Outline each Plasmodium ovale-infected red blood cell.
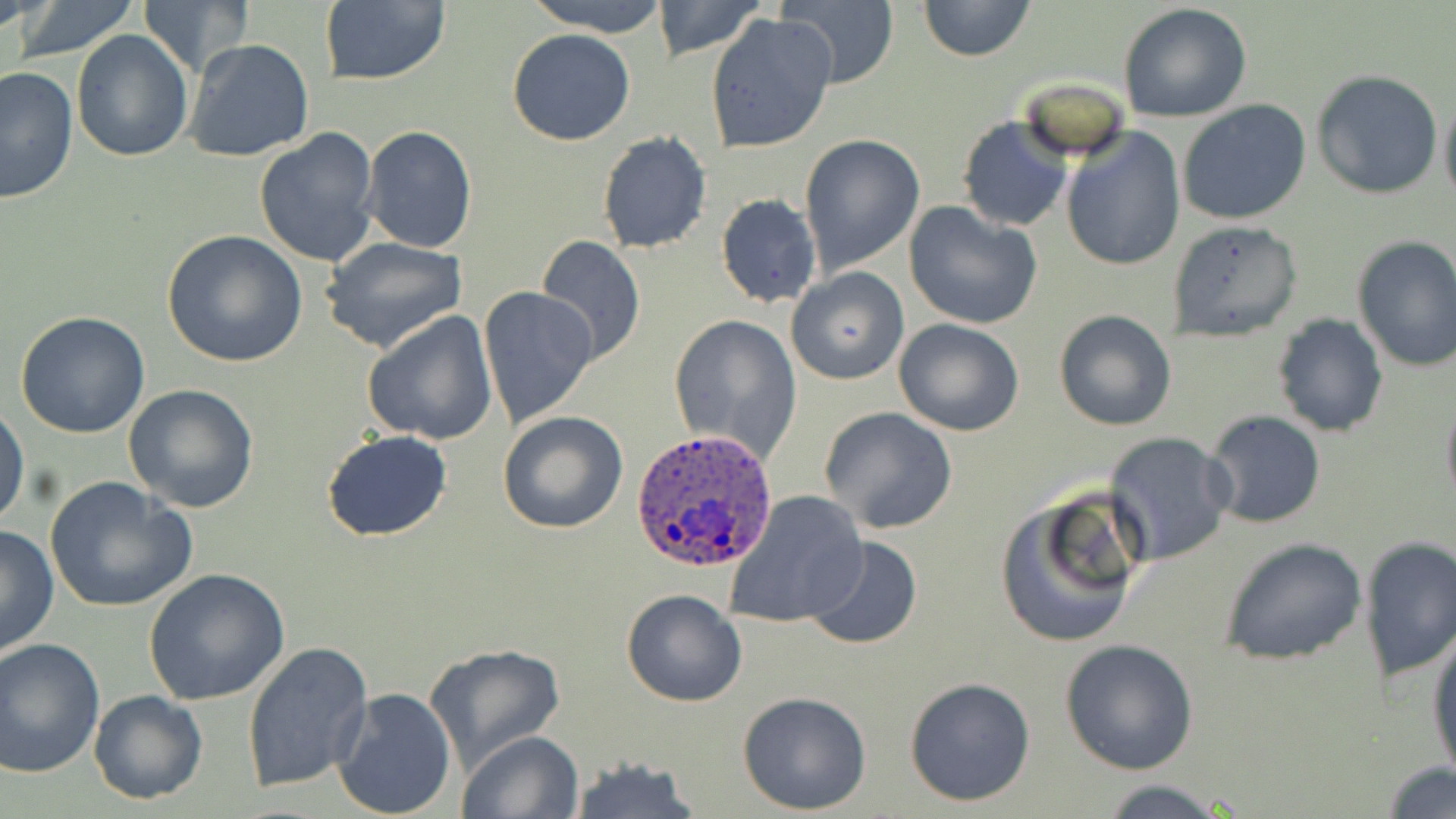

Approximate bounding boxes as (x1,y1)-(x2,y2) corner pairs in pixels.
Plasmodium ovale-infected red blood cells: (629,430)-(778,572).

Summary:
  - Uninfected red blood cell locations: (11,0)-(144,61), (524,0)-(676,36), (650,0)-(767,60), (918,0)-(1036,63), (139,1)-(251,73), (317,1)-(452,87), (777,1)-(897,86), (1118,2)-(1254,124), (704,12)-(837,154), (507,29)-(636,146), (70,30)-(193,161), (184,38)-(316,164), (1,67)-(78,204), (1312,69)-(1444,197), (1439,91)-(1456,212), (1177,99)-(1312,225), (956,115)-(1073,233), (361,126)-(477,253), (254,127)-(380,268), (1060,128)-(1186,272), (597,132)-(713,255), (798,134)-(925,274), (708,174)-(905,301), (715,193)-(822,308), (904,200)-(1042,330), (1167,219)-(1303,342), (161,229)-(307,368), (1351,234)-(1456,373), (535,235)-(646,368), (319,236)-(470,355), (785,267)-(908,386), (478,287)-(600,430), (1053,308)-(1177,431), (360,310)-(498,446), (13,312)-(152,439), (668,312)-(803,461), (1272,312)-(1388,437), (894,318)-(1025,437), (121,383)-(261,515), (1440,390)-(1456,512), (1,403)-(27,527), (820,407)-(958,535), (1204,410)-(1327,529), (498,411)-(628,534), (322,430)-(452,542), (1104,431)-(1234,567), (45,476)-(197,615), (993,489)-(1145,648), (722,491)-(869,630), (0,524)-(59,657), (805,535)-(922,651), (1357,535)-(1456,686), (1218,537)-(1369,666), (145,567)-(290,706), (621,588)-(748,707), (1427,626)-(1456,782), (0,636)-(105,779), (1060,638)-(1201,775), (242,640)-(373,794), (424,642)-(566,773), (903,677)-(1035,807), (332,685)-(456,817), (88,689)-(209,805), (737,690)-(873,814), (458,729)-(584,819), (566,757)-(701,818), (1382,761)-(1456,818), (1089,778)-(1241,819)
  - Slide-level diagnosis: Plasmodium ovale
  - Image size: 1456×819 pixels
  - Preparation: thin blood smear
  - Modality: light microscopy
  - Field of view: single
  - Stain: May-Grünwald-Giemsa
  - Magnification: 1000x